Describe the morphology of the erythrocytes.
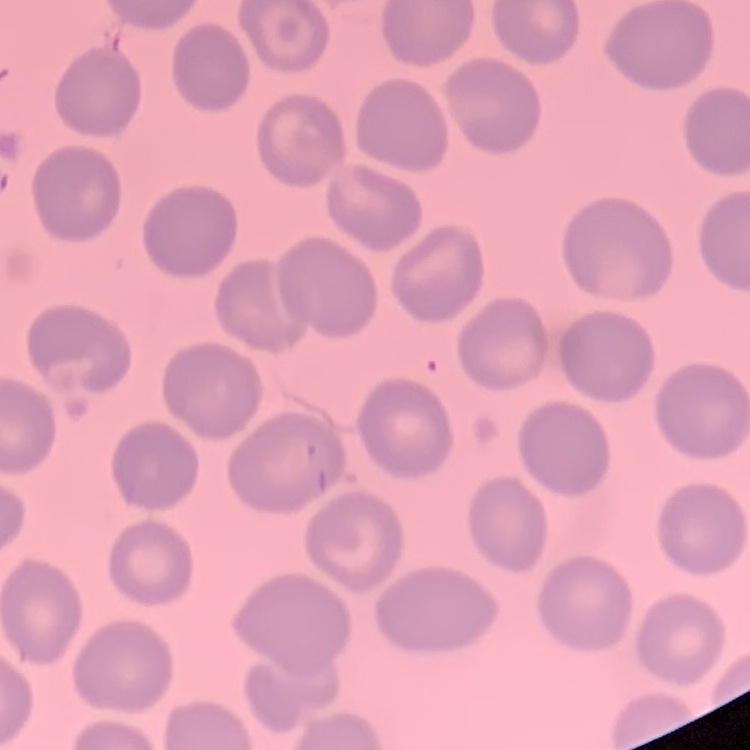

No rouleaux formation.

preparation = thin blood film
image type = square crop of a larger photomicrograph
stain = Field's or Giemsa